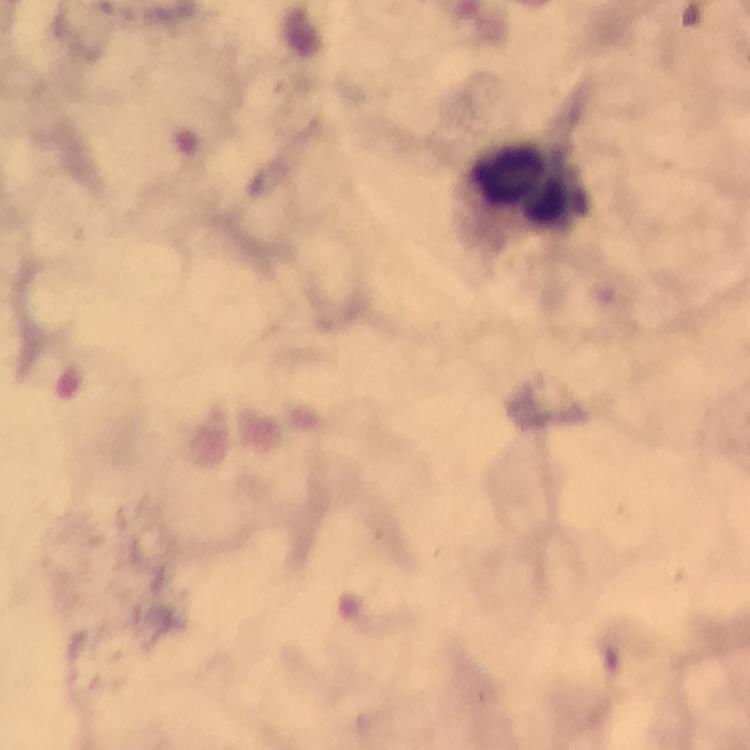
cropped from = one field of view
stain = Giemsa
preparation = thick blood smear
magnification = 100x
immersion oil = applied
leukocyte locations = approximate centers as (x, y) in pixels: (530, 192)
image size = 750×750 pixels
context = from a malaria diagnostic workup
Plasmodium parasites = none detected
capture = smartphone photograph through a microscope